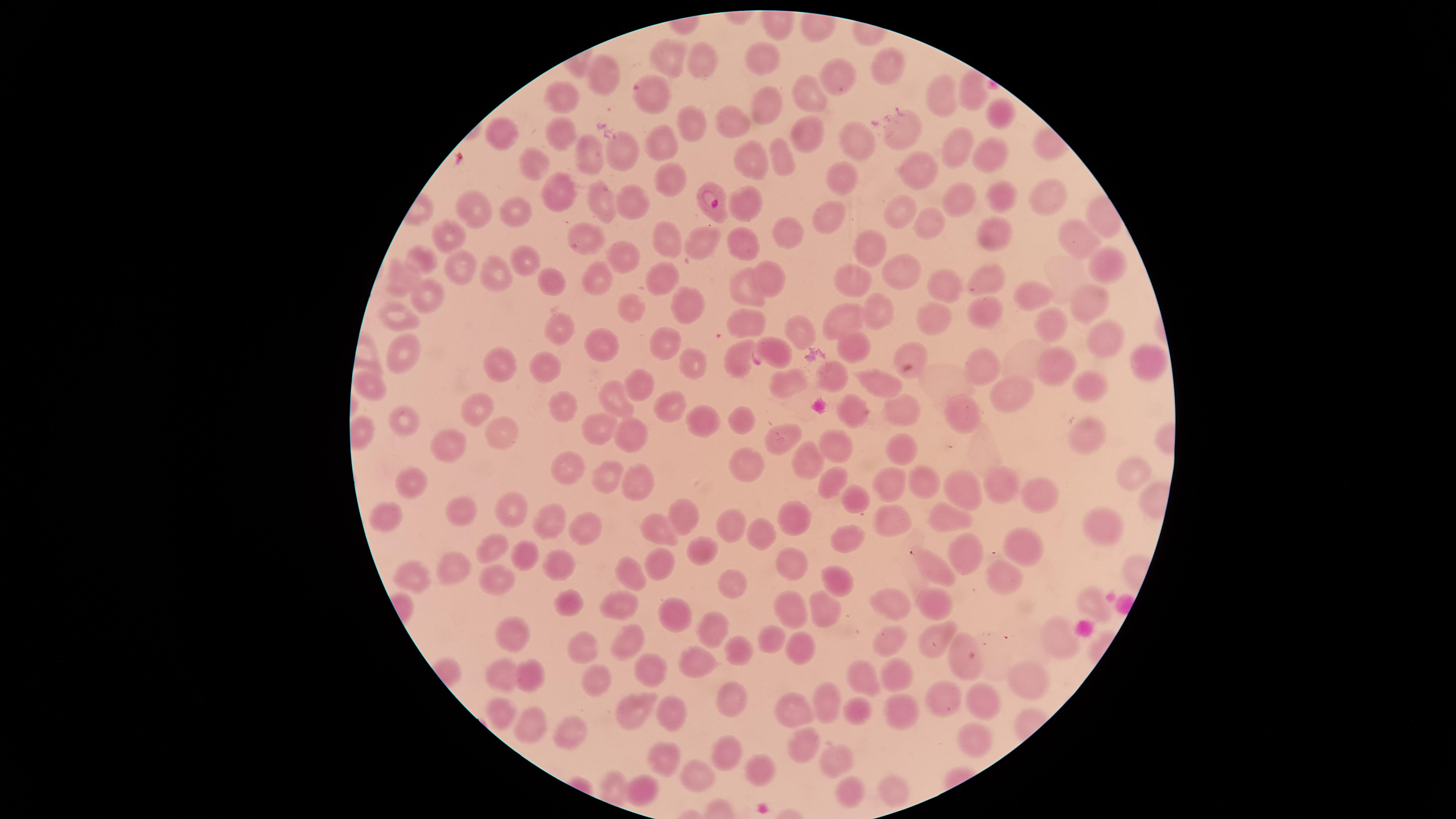 Approximate marker points, in pixels from the top-left corner. Uninfected red blood cells: (x=671, y=57), (x=704, y=59), (x=765, y=59), (x=889, y=66), (x=838, y=78), (x=809, y=92), (x=972, y=95), (x=654, y=97), (x=561, y=98), (x=938, y=98), (x=772, y=108), (x=997, y=113), (x=687, y=123), (x=736, y=123), (x=905, y=129), (x=805, y=130), (x=567, y=136), (x=504, y=137), (x=852, y=138), (x=665, y=139), (x=616, y=147), (x=951, y=147), (x=986, y=153), (x=589, y=159), (x=777, y=160), (x=759, y=161), (x=537, y=164), (x=923, y=167), (x=665, y=175), (x=847, y=179), (x=559, y=192), (x=1048, y=199), (x=598, y=201), (x=999, y=202), (x=747, y=203), (x=965, y=203), (x=629, y=205), (x=906, y=211), (x=475, y=212), (x=831, y=212), (x=516, y=214), (x=928, y=225), (x=990, y=231), (x=789, y=233), (x=585, y=234), (x=1074, y=234), (x=448, y=237), (x=668, y=239), (x=704, y=241), (x=741, y=241), (x=870, y=250), (x=622, y=258), (x=521, y=260), (x=425, y=261), (x=1103, y=264), (x=464, y=269), (x=905, y=273), (x=771, y=276), (x=491, y=277), (x=664, y=278), (x=986, y=279), (x=404, y=280), (x=595, y=281), (x=550, y=282), (x=857, y=282), (x=953, y=287), (x=748, y=289), (x=1033, y=295), (x=428, y=298), (x=1088, y=302), (x=687, y=303), (x=638, y=307), (x=981, y=311), (x=885, y=317), (x=400, y=318), (x=859, y=318), (x=748, y=322), (x=937, y=324), (x=1050, y=324), (x=556, y=329), (x=802, y=331), (x=1101, y=336), (x=599, y=342), (x=667, y=345), (x=847, y=346), (x=780, y=350), (x=908, y=351), (x=403, y=352), (x=736, y=355), (x=1144, y=361), (x=695, y=362), (x=509, y=363), (x=984, y=365), (x=1060, y=365), (x=547, y=369), (x=826, y=369), (x=882, y=383), (x=787, y=384), (x=1084, y=385), (x=643, y=387), (x=374, y=389), (x=1002, y=391), (x=671, y=397), (x=562, y=399), (x=621, y=400), (x=852, y=407), (x=479, y=410), (x=904, y=410), (x=405, y=418), (x=706, y=419), (x=739, y=419), (x=970, y=419), (x=600, y=426), (x=494, y=432), (x=631, y=435), (x=1085, y=435), (x=784, y=438), (x=837, y=441), (x=454, y=442), (x=901, y=452), (x=807, y=459), (x=747, y=460), (x=575, y=469), (x=633, y=471), (x=1128, y=473), (x=828, y=475), (x=609, y=478), (x=413, y=483), (x=1005, y=483), (x=889, y=485), (x=926, y=487), (x=969, y=489), (x=1036, y=490), (x=856, y=499), (x=512, y=501), (x=458, y=506), (x=951, y=513), (x=889, y=515), (x=388, y=516), (x=684, y=516), (x=800, y=516), (x=554, y=524), (x=585, y=525), (x=1108, y=525), (x=726, y=527), (x=663, y=528), (x=765, y=534), (x=845, y=537), (x=958, y=545), (x=1016, y=545), (x=498, y=546), (x=697, y=548), (x=523, y=551), (x=562, y=562), (x=663, y=566), (x=460, y=567), (x=790, y=568), (x=940, y=570), (x=1008, y=572), (x=499, y=573), (x=417, y=576), (x=627, y=576), (x=838, y=578), (x=737, y=581), (x=565, y=596), (x=1090, y=599), (x=623, y=600), (x=891, y=602), (x=933, y=603), (x=671, y=608), (x=796, y=608), (x=831, y=613), (x=707, y=619), (x=509, y=631), (x=892, y=636), (x=935, y=636), (x=629, y=637), (x=766, y=641), (x=1067, y=642), (x=585, y=645), (x=804, y=646), (x=703, y=654), (x=741, y=655), (x=956, y=664), (x=650, y=667), (x=505, y=669), (x=893, y=674), (x=534, y=676), (x=860, y=677), (x=599, y=678), (x=1028, y=680), (x=729, y=696), (x=984, y=697), (x=949, y=700), (x=830, y=701), (x=630, y=705), (x=791, y=709), (x=849, y=711), (x=905, y=712), (x=499, y=715), (x=670, y=715), (x=531, y=721), (x=574, y=725), (x=980, y=737), (x=802, y=745), (x=726, y=751), (x=657, y=760), (x=835, y=760), (x=759, y=765), (x=705, y=776), (x=644, y=786), (x=888, y=790), (x=848, y=791). Parasitized red blood cells: (x=712, y=194). Presence: malaria parasites seen. The visible region is circular. Giemsa stain. Single field of view. Smartphone photograph through the microscope eyepiece. Thin blood film. Image is 1456×819 pixels. Species: Plasmodium falciparum.